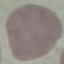

{
  "malaria_status": "uninfected",
  "capture": "smartphone through the microscope eyepiece",
  "image_type": "cell patch, automatically extracted from a larger field of view and resized to 64 × 64 pixels",
  "stain": "Giemsa",
  "preparation": "thin smear"
}